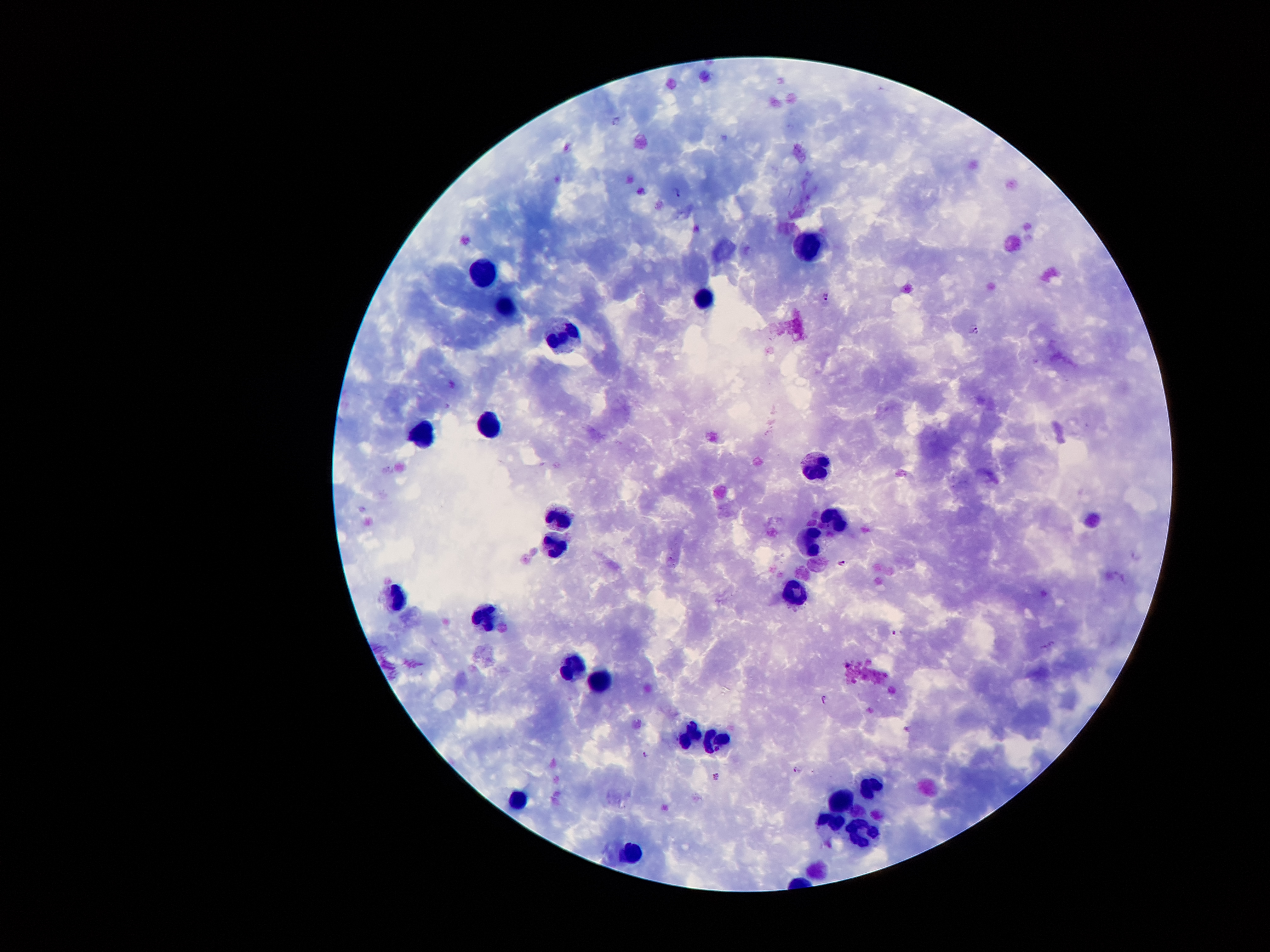

Approximate centers as {x, y} in pixels.
Summary:
  - Leukocyte locations: {808, 244}, {484, 269}, {703, 301}, {506, 307}, {560, 335}, {488, 427}, {419, 435}, {813, 467}, {557, 516}, {835, 519}, {810, 540}, {553, 543}, {796, 593}, {398, 598}, {482, 614}, {579, 662}, {599, 677}, {691, 733}, {719, 741}, {871, 787}, {842, 797}, {515, 802}, {825, 824}, {865, 834}, {628, 855}
  - Plasmodium parasite locations: {618, 120}, {678, 193}, {826, 296}, {975, 329}, {843, 562}, {894, 633}, {824, 698}, {646, 753}, {798, 769}, {717, 777}
  - Magnification: 100x
  - Stain: Giemsa
  - Image size: 1270×952 pixels
  - Capture: smartphone camera through the microscope eyepiece
  - Preparation: thick blood smear
  - Patient malaria status: positive for Plasmodium falciparum
  - Field of view: single